Identify the parasite.
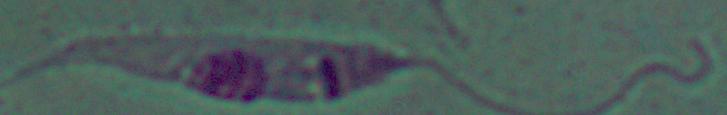

Leishmania.

Summary:
  - Magnification: 1000x
  - Modality: photomicrograph